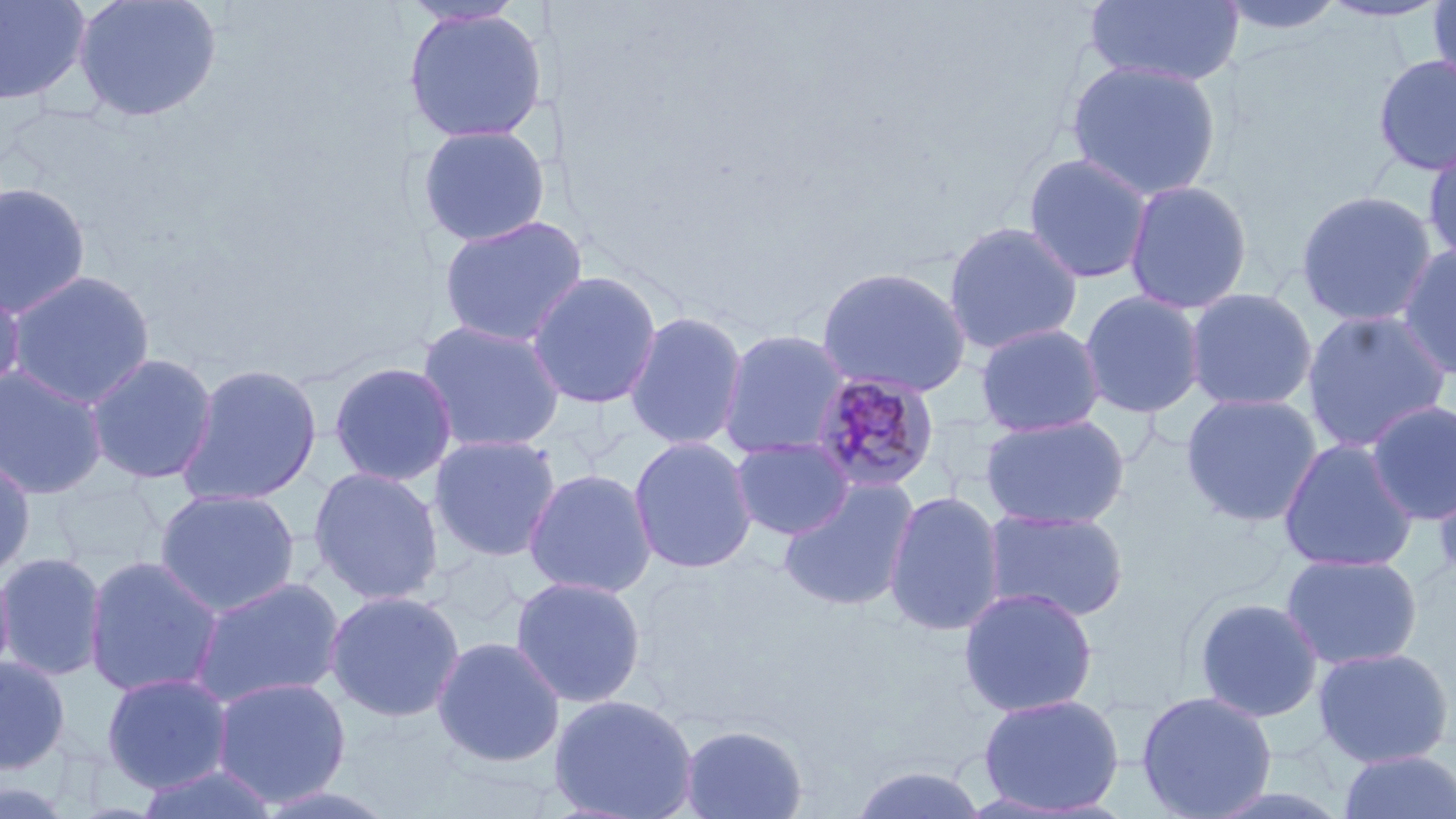

slide_level_diagnosis: Plasmodium malariae
stain: May-Grünwald-Giemsa
magnification: 1000x
preparation: thin blood smear
field_of_view: single
uninfected_red_blood_cell_locations: 'approximate bounding boxes as [x1, y1, x2, y2] in pixels: [0, 0, 91, 107], [72, 0, 223, 123], [1084, 0, 1245, 87], [1215, 0, 1348, 38], [1426, 0, 1456, 90], [1316, 1, 1453, 24], [403, 7, 548, 145], [1371, 53, 1456, 177], [1065, 59, 1222, 202], [416, 124, 551, 247], [1422, 143, 1456, 268], [1021, 152, 1155, 285], [1122, 179, 1253, 315], [0, 181, 93, 319], [1295, 189, 1439, 328], [436, 214, 589, 348], [942, 220, 1084, 355], [1396, 243, 1456, 381], [815, 265, 972, 398], [4, 269, 157, 410], [527, 269, 663, 410], [0, 279, 26, 404], [1185, 287, 1318, 412], [1079, 290, 1207, 418], [1301, 309, 1452, 453], [624, 310, 749, 451], [416, 319, 567, 454], [975, 322, 1106, 437], [717, 328, 852, 461], [85, 352, 219, 485], [328, 361, 459, 487], [176, 362, 323, 506], [0, 365, 109, 499], [1181, 392, 1323, 527], [1365, 400, 1456, 524], [979, 414, 1130, 529], [428, 434, 562, 563], [628, 436, 758, 574], [730, 436, 855, 540], [1278, 437, 1419, 573], [0, 455, 37, 580], [1431, 456, 1456, 590], [307, 467, 445, 606], [522, 467, 658, 598], [778, 477, 920, 613], [153, 488, 302, 618], [884, 489, 1007, 637], [981, 507, 1131, 623], [0, 552, 107, 682], [1280, 552, 1423, 670], [83, 555, 225, 699], [0, 561, 16, 689], [509, 575, 647, 709], [188, 576, 347, 709], [958, 587, 1099, 718], [325, 589, 466, 723], [1192, 597, 1324, 723], [431, 636, 566, 767], [1311, 645, 1455, 768], [0, 656, 70, 774], [100, 671, 234, 793], [210, 676, 352, 808], [1135, 690, 1278, 819], [977, 692, 1126, 815], [548, 694, 699, 819], [679, 724, 808, 819], [1336, 749, 1456, 819], [132, 763, 281, 819], [848, 765, 990, 819], [0, 778, 77, 818], [250, 784, 403, 818]'
modality: light microscopy
image_size: 1456×819 pixels
plasmodium_malariae_infected_red_blood_cell_locations: 'approximate bounding boxes as [x1, y1, x2, y2] in pixels: [808, 371, 941, 494]'